Give the extent of all Plasmodium falciparum-infected red blood cells.
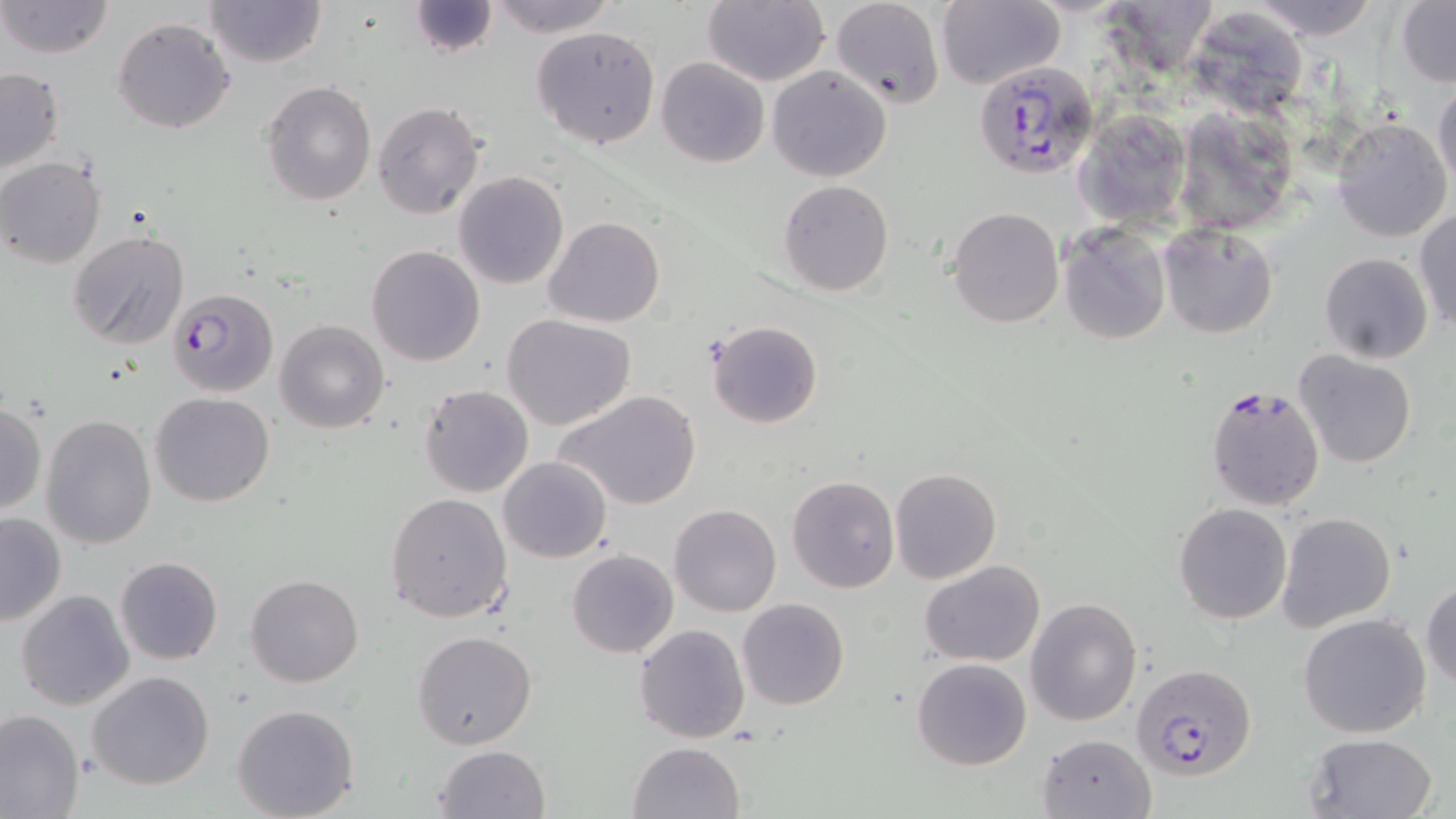
Approximate bounding boxes as (x1,y1)-(x2,y2) corner pairs in pixels.
Plasmodium falciparum-infected red blood cells: (973,60)-(1099,178), (168,288)-(279,397), (1203,382)-(1328,512), (1134,665)-(1255,778).

slide-level diagnosis = Plasmodium falciparum
magnification = 1000x
modality = light microscopy
uninfected red blood cell locations = approximate bounding boxes as (x1,y1)-(x2,y2) corner pairs in pixels: (0,0)-(115,59), (203,0)-(326,69), (485,0)-(622,37), (702,0)-(830,87), (830,0)-(945,110), (1239,0)-(1385,40), (407,1)-(499,58), (1094,1)-(1221,83), (937,2)-(1064,89), (1395,2)-(1456,85), (112,16)-(236,134), (1203,16)-(1306,121), (531,25)-(660,150), (656,57)-(770,168), (767,67)-(892,182), (0,68)-(64,175), (259,80)-(377,206), (1433,80)-(1456,193), (372,102)-(485,219), (1076,107)-(1191,228), (1180,116)-(1307,243), (1331,117)-(1451,243), (0,157)-(105,269), (453,171)-(569,289), (778,180)-(893,297), (947,207)-(1064,327), (1414,211)-(1455,332), (543,216)-(665,328), (1157,221)-(1277,340), (1059,223)-(1172,344), (68,229)-(192,351), (367,245)-(486,367), (1319,252)-(1433,362), (502,314)-(636,430), (704,319)-(824,429), (276,320)-(389,435), (1292,350)-(1418,471), (419,384)-(535,498), (555,389)-(702,513), (151,392)-(275,508), (0,401)-(46,515), (42,415)-(157,551), (499,457)-(612,562), (889,466)-(1001,585), (787,475)-(899,592), (385,493)-(514,624), (669,502)-(781,616), (1173,502)-(1292,624), (1276,511)-(1396,631), (0,512)-(67,626), (567,549)-(678,660), (114,555)-(223,666), (918,560)-(1045,665), (245,574)-(364,688), (1421,579)-(1455,689), (15,590)-(134,710), (1025,596)-(1143,725), (737,598)-(849,710), (1299,613)-(1431,739), (633,623)-(751,744), (412,630)-(538,751), (911,657)-(1033,770), (87,670)-(216,790), (231,703)-(361,819), (0,709)-(84,818), (1036,731)-(1157,819), (1302,733)-(1439,818), (627,741)-(745,819), (432,745)-(549,819)
stain = May-Grünwald-Giemsa
image size = 1456×819 pixels
field of view = single
preparation = thin blood film